Locate and identify every blood parasite.
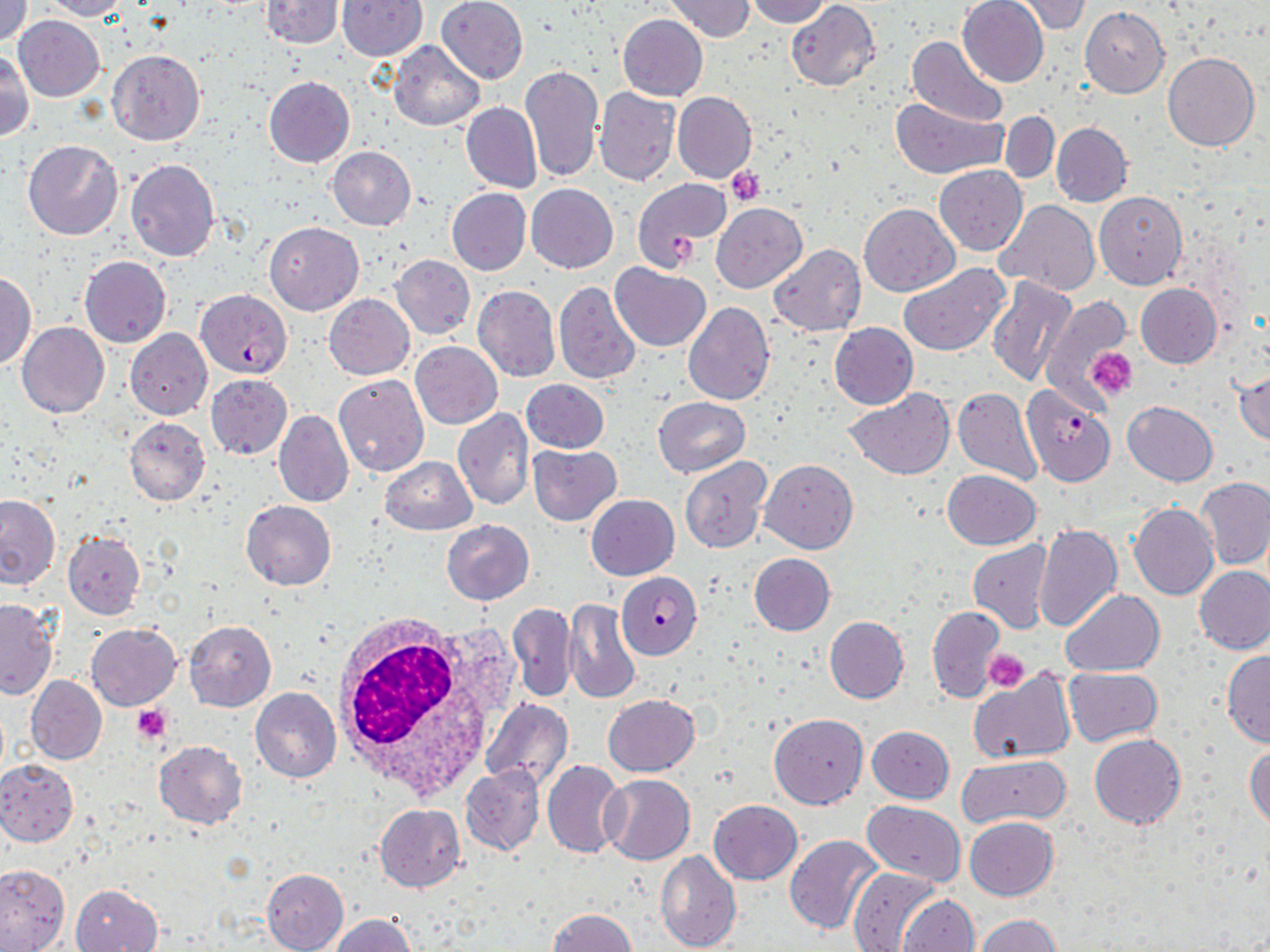
Approximate bounding boxes as (x1, y1, x2, y2) in pixels.
Plasmodium falciparum-infected red blood cells: (196, 290, 291, 377), (1021, 384, 1117, 485), (616, 572, 702, 658).
No Plasmodium ovale, Plasmodium malariae, Plasmodium vivax, Babesia divergens, or Trypanosoma brucei observed.

Summary:
  - Platelet locations: (726, 166, 766, 206), (668, 234, 702, 266), (1087, 347, 1137, 398), (983, 650, 1029, 694), (131, 705, 173, 742)
  - White blood cell locations: (328, 611, 519, 799)
  - Uninfected red blood cell locations: (1, 0, 32, 46), (42, 0, 130, 21), (260, 0, 343, 48), (436, 0, 528, 84), (665, 0, 755, 42), (745, 0, 830, 26), (958, 0, 1049, 87), (1012, 0, 1091, 36), (337, 1, 428, 60), (786, 1, 879, 90), (1080, 7, 1169, 97), (617, 14, 708, 101), (13, 16, 105, 101), (908, 36, 1009, 127), (387, 42, 484, 131), (1, 50, 34, 141), (107, 50, 205, 146), (1163, 51, 1259, 152), (520, 64, 604, 182), (263, 76, 355, 167), (594, 87, 681, 185), (672, 91, 757, 184), (891, 97, 1009, 181), (462, 103, 542, 194), (1001, 111, 1058, 183), (1050, 121, 1133, 206), (22, 139, 123, 239), (327, 145, 416, 230), (125, 159, 220, 261), (934, 165, 1028, 256), (632, 177, 732, 270), (526, 183, 618, 273), (446, 188, 530, 275), (1094, 191, 1187, 289), (995, 201, 1099, 296), (711, 203, 806, 293), (859, 203, 960, 296), (264, 221, 364, 315), (770, 245, 866, 337), (391, 255, 474, 339), (79, 256, 171, 347), (900, 263, 1009, 357), (612, 264, 712, 352), (51, 269, 156, 379), (0, 272, 37, 367), (988, 277, 1076, 387), (554, 279, 641, 383), (1135, 284, 1222, 367), (472, 285, 559, 382), (324, 295, 414, 378), (1039, 297, 1131, 404), (683, 302, 775, 404), (17, 321, 109, 418), (829, 322, 918, 409), (126, 329, 212, 419), (411, 342, 502, 428), (1233, 368, 1270, 447), (206, 374, 292, 460), (334, 374, 429, 476), (520, 379, 609, 453), (953, 388, 1043, 486), (846, 389, 952, 480), (653, 397, 749, 477), (1122, 400, 1217, 486), (452, 408, 534, 511), (274, 409, 353, 507), (124, 417, 210, 505), (528, 444, 621, 526), (379, 457, 477, 534), (679, 458, 771, 553), (760, 460, 857, 554), (955, 469, 1043, 628), (941, 470, 1039, 550), (1197, 477, 1270, 570), (586, 494, 678, 580), (0, 496, 60, 590), (241, 500, 336, 590), (1128, 503, 1219, 600), (441, 520, 534, 605), (1033, 523, 1122, 632), (62, 531, 145, 620), (967, 541, 1052, 633), (748, 553, 835, 636), (1195, 566, 1270, 655), (1060, 589, 1165, 677), (0, 598, 58, 700), (565, 599, 641, 704), (507, 603, 577, 702), (927, 606, 1004, 702), (825, 616, 909, 703), (184, 620, 276, 711), (86, 623, 181, 711), (1221, 650, 1270, 747), (969, 667, 1077, 764), (1062, 667, 1163, 747), (26, 677, 106, 764), (250, 687, 342, 783), (603, 694, 699, 776), (481, 699, 572, 792), (769, 713, 868, 809), (866, 725, 954, 803), (1090, 734, 1186, 829), (154, 740, 247, 828), (1245, 744, 1270, 830), (957, 756, 1069, 828), (0, 759, 78, 846), (542, 760, 626, 859), (461, 765, 544, 856), (599, 774, 694, 865), (709, 799, 802, 884), (863, 801, 966, 887), (374, 804, 466, 892), (964, 817, 1058, 900), (785, 835, 885, 934), (656, 850, 741, 951), (0, 863, 69, 951), (845, 867, 939, 951), (261, 868, 349, 952), (71, 884, 161, 951), (896, 895, 978, 951), (546, 908, 637, 952), (330, 914, 417, 951), (975, 914, 1062, 951)
  - Slide-level diagnosis: Plasmodium falciparum
  - Modality: optical microscopy
  - Image size: 1270×952 pixels
  - Field of view: one of a larger specimen
  - Stain: May-Grünwald-Giemsa
  - Preparation: thin blood film
  - Magnification: 1000x